Classify this cell by malaria status.
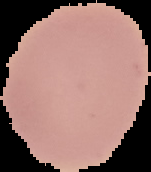
It is uninfected.

Summary:
  - Preparation: thin blood smear
  - Image type: segmented cell region on a black background
  - Image size: 151×172 pixels